Classify this cell by malaria status.
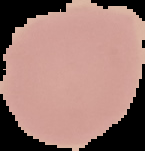

It is uninfected.

Segmented cell region on a black background. From a thin blood smear. Image is 145×151 pixels.